State the preparation type.
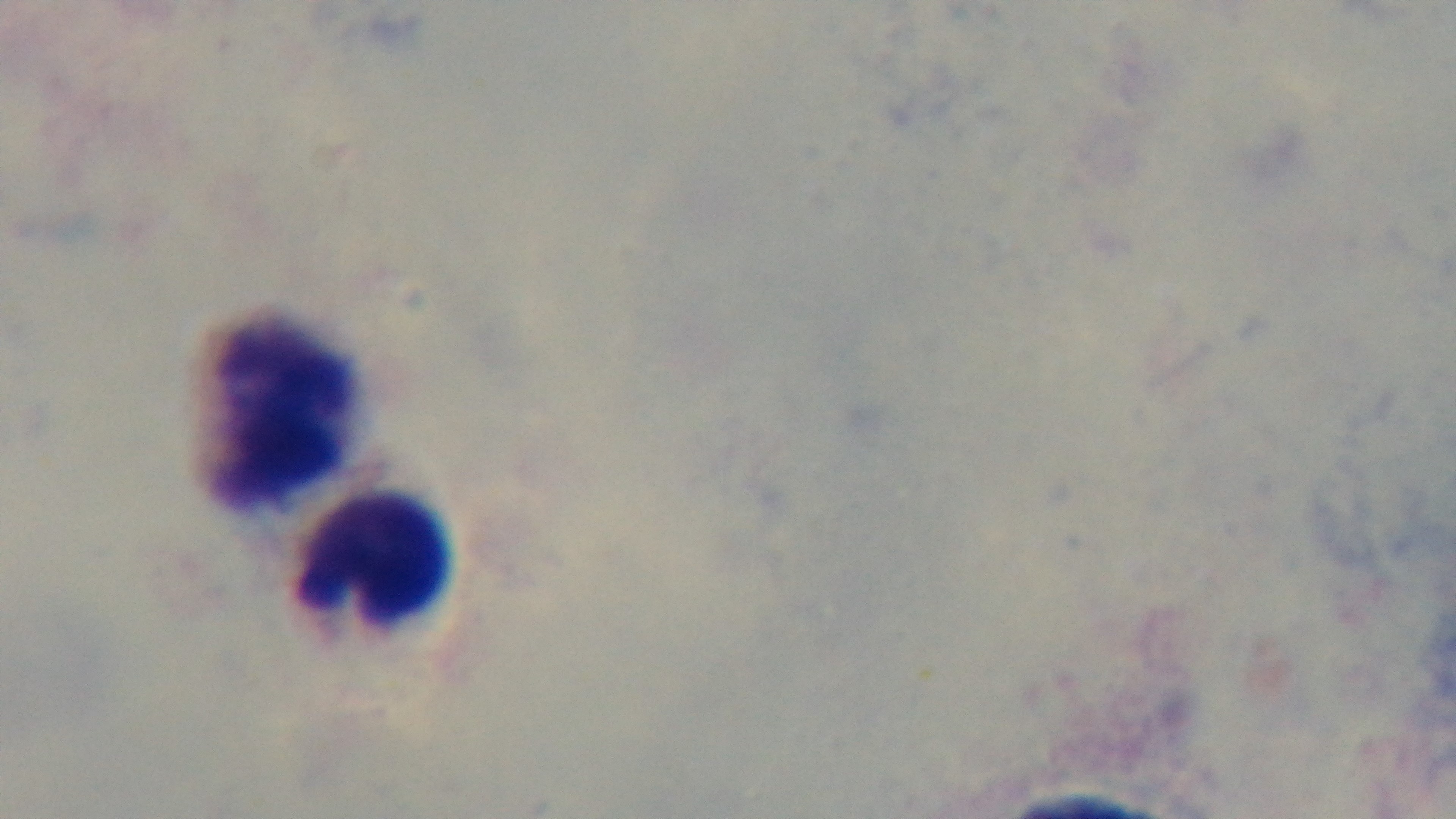
It is a thick blood film.

Single field of view. Giemsa-stained. Malaria status: negative. Captured with a mounted 4K digital camera. Oil-immersion objective, 100x. Photomicrograph.